Assess this cell for malaria.
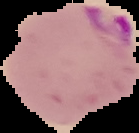

It is parasitized.

preparation = thin blood smear
image size = 139×133 pixels
image type = segmented cell region on a black background